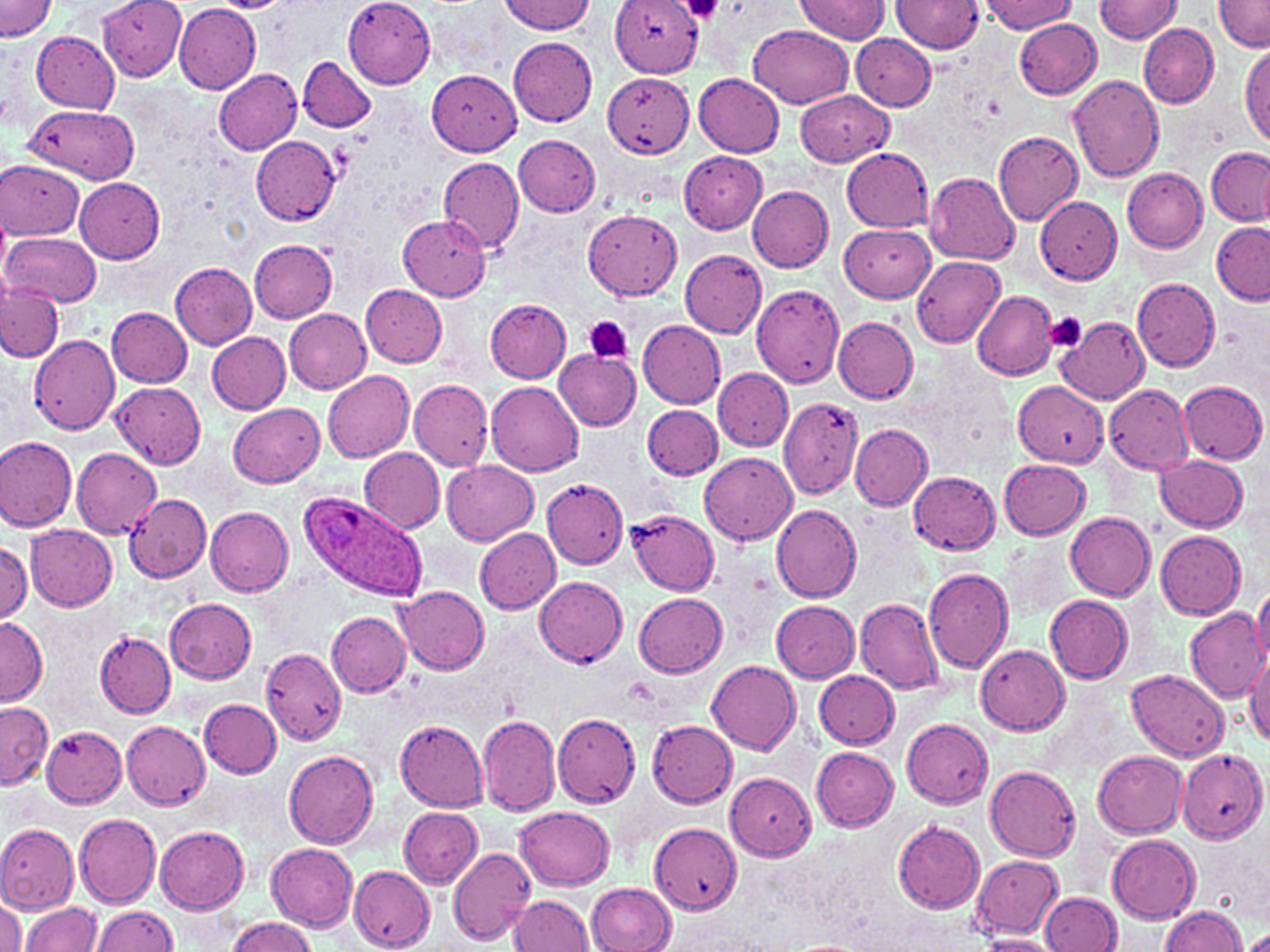
Approximate bounding boxes as [x1, y1, x2, y2] in pixels. Platelet locations: [679, 0, 730, 22], [1045, 312, 1088, 351], [583, 315, 631, 363]. Plasmodium ovale-infected red blood cell locations: [297, 491, 429, 601]. Uninfected red blood cell locations: [0, 0, 55, 38], [96, 0, 185, 80], [343, 0, 435, 89], [500, 0, 595, 36], [610, 0, 705, 77], [796, 0, 890, 43], [890, 0, 984, 54], [981, 0, 1077, 35], [1215, 0, 1270, 51], [1094, 1, 1182, 42], [174, 4, 261, 94], [1013, 18, 1101, 98], [1138, 24, 1219, 108], [748, 26, 856, 109], [32, 32, 119, 112], [850, 33, 937, 111], [509, 38, 597, 127], [1242, 45, 1270, 147], [298, 57, 375, 133], [214, 69, 302, 154], [428, 69, 523, 156], [603, 72, 692, 158], [695, 74, 784, 157], [1067, 74, 1165, 183], [795, 90, 893, 165], [27, 105, 141, 183], [994, 131, 1083, 224], [514, 135, 599, 216], [251, 136, 340, 224], [1206, 147, 1270, 225], [842, 148, 934, 230], [678, 150, 767, 232], [437, 155, 523, 254], [0, 160, 84, 239], [696, 165, 834, 257], [1123, 168, 1207, 252], [924, 173, 1020, 263], [74, 176, 165, 263], [748, 186, 833, 272], [1035, 195, 1122, 284], [582, 209, 682, 299], [398, 216, 489, 300], [1211, 221, 1270, 304], [839, 224, 935, 301], [5, 232, 100, 306], [249, 240, 337, 322], [680, 250, 767, 338], [912, 256, 1005, 348], [170, 263, 257, 349], [1132, 277, 1220, 372], [752, 282, 841, 387], [1, 285, 63, 362], [361, 285, 447, 366], [972, 290, 1060, 380], [485, 299, 572, 383], [106, 307, 193, 387], [283, 308, 371, 394], [1057, 316, 1150, 404], [833, 317, 917, 403], [638, 321, 725, 408], [208, 332, 291, 414], [29, 334, 120, 435], [556, 350, 640, 430], [713, 368, 793, 450], [323, 370, 415, 462], [409, 377, 492, 472], [1179, 380, 1267, 463], [487, 381, 583, 477], [111, 382, 206, 469], [1013, 382, 1108, 466], [1103, 385, 1194, 475], [778, 398, 864, 501], [228, 403, 324, 486], [643, 405, 722, 480], [851, 424, 933, 510], [0, 436, 78, 531], [359, 446, 444, 534], [72, 447, 162, 538], [700, 452, 797, 545], [1155, 454, 1248, 531], [441, 459, 538, 545], [999, 459, 1090, 540], [909, 472, 1001, 553], [542, 478, 627, 570], [125, 493, 213, 581], [771, 502, 862, 603], [205, 506, 293, 595], [628, 509, 719, 595], [1066, 512, 1154, 600], [1058, 514, 1147, 683], [25, 524, 118, 610], [475, 527, 561, 612], [1156, 530, 1246, 619], [1, 540, 33, 623], [923, 567, 1013, 673], [535, 577, 627, 667], [1252, 584, 1270, 669], [395, 586, 489, 673], [634, 593, 727, 677], [1046, 596, 1132, 684], [855, 597, 945, 694], [166, 598, 256, 682], [771, 601, 860, 681], [1186, 608, 1267, 701], [327, 612, 410, 697], [1, 615, 46, 704], [94, 632, 177, 717], [976, 644, 1069, 735], [262, 651, 347, 743], [1245, 653, 1270, 746], [708, 660, 801, 753], [1127, 669, 1229, 762], [813, 671, 898, 748], [199, 699, 281, 777], [1, 703, 52, 789], [553, 711, 641, 807], [477, 716, 560, 816], [901, 717, 993, 805], [393, 718, 489, 811], [646, 719, 737, 805], [121, 721, 210, 810], [40, 724, 128, 808], [282, 748, 379, 849], [810, 748, 898, 831], [1179, 749, 1267, 841], [1093, 750, 1187, 837], [985, 765, 1083, 862], [725, 773, 815, 861], [514, 806, 614, 890], [399, 807, 482, 887], [75, 813, 161, 909], [893, 821, 985, 913], [0, 822, 78, 914], [650, 822, 741, 912], [154, 824, 250, 914], [1108, 835, 1200, 922], [267, 843, 358, 931], [447, 847, 537, 945], [971, 855, 1064, 938], [350, 866, 434, 952], [587, 882, 674, 951], [1040, 892, 1121, 952], [510, 895, 592, 950], [0, 898, 25, 952], [19, 902, 100, 952], [93, 904, 179, 951], [1158, 906, 1247, 951], [229, 917, 318, 952], [1241, 928, 1270, 952], [976, 934, 1061, 952]. Slide-level diagnosis: Plasmodium ovale. Light microscopy. Thin blood film. May-Grünwald-Giemsa-stained preparation. One field of a larger specimen. 1000x magnification. Image is 1270×952 pixels.